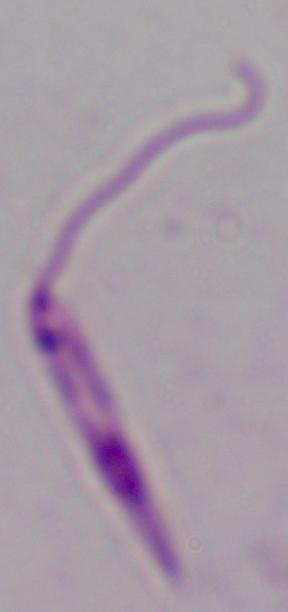
identification: Leishmania
magnification: 1000x
modality: photomicrograph